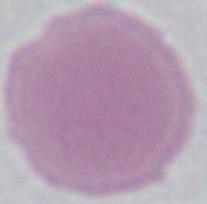
magnification: 1000x
modality: photomicrograph
identification: red blood cell